Locate every Plasmodium vivax-infected red blood cell.
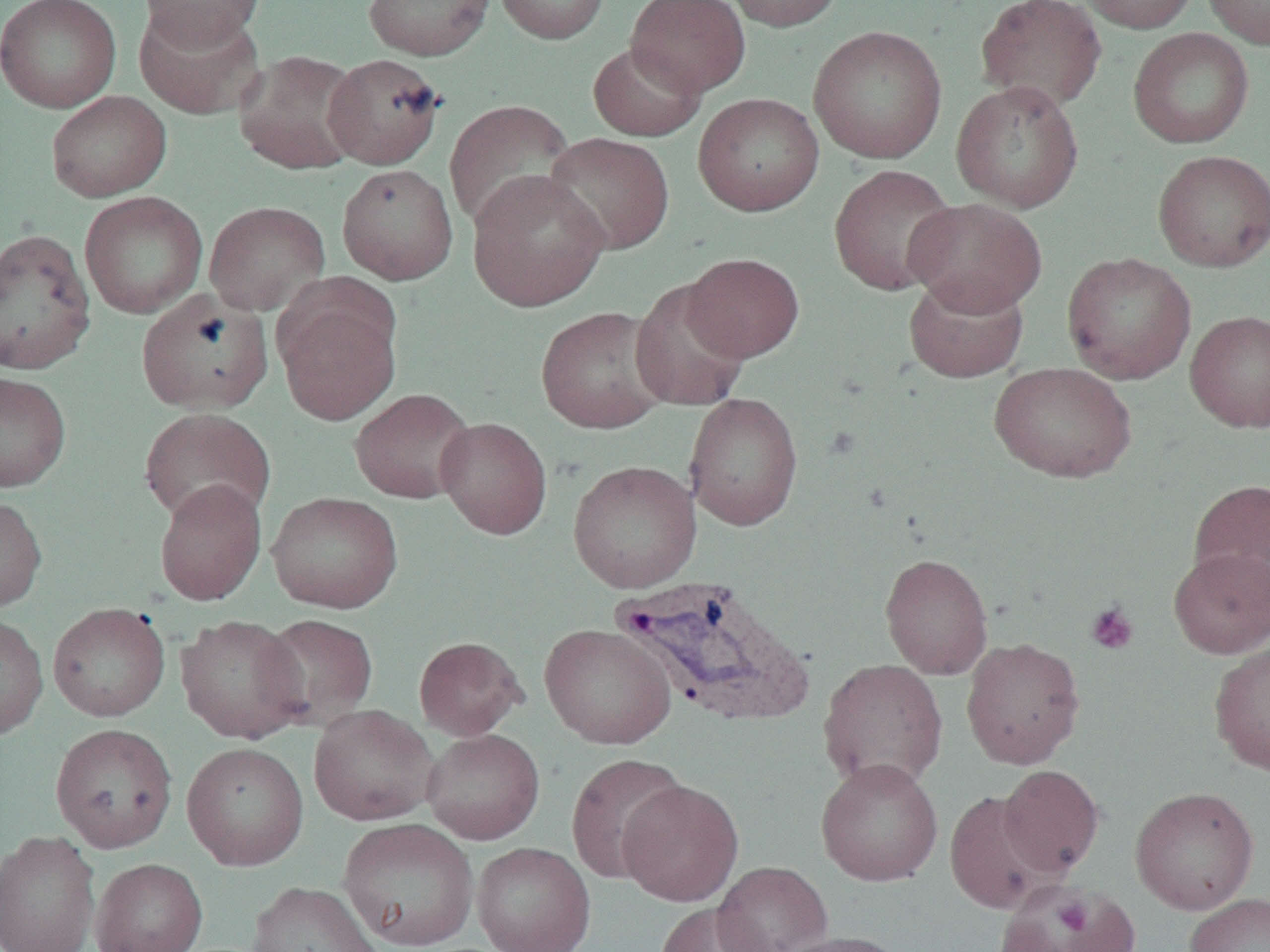
Approximate bounding boxes as [x1, y1, x2, y2] in pixels.
Plasmodium vivax-infected red blood cells: [610, 576, 815, 726].

slide-level diagnosis = Plasmodium vivax
magnification = 1000x
platelet locations = approximate bounding boxes as [x1, y1, x2, y2] in pixels: [1085, 602, 1139, 655], [1051, 895, 1097, 939]
modality = light microscopy
uninfected red blood cell locations = approximate bounding boxes as [x1, y1, x2, y2] in pixels: [0, 0, 122, 113], [138, 0, 267, 48], [362, 0, 496, 61], [493, 0, 611, 45], [626, 0, 751, 97], [723, 0, 846, 32], [974, 0, 1107, 113], [1077, 0, 1200, 34], [1202, 0, 1270, 49], [133, 3, 266, 119], [808, 26, 947, 164], [1128, 28, 1254, 149], [588, 41, 706, 142], [233, 49, 366, 175], [323, 52, 446, 169], [951, 79, 1084, 213], [46, 91, 172, 202], [693, 92, 824, 216], [444, 98, 576, 232], [542, 132, 675, 255], [1152, 149, 1270, 271], [336, 163, 458, 285], [828, 164, 959, 296], [466, 169, 610, 312], [79, 191, 207, 318], [902, 197, 1048, 317], [204, 201, 331, 316], [0, 228, 97, 375], [682, 252, 805, 362], [1061, 252, 1197, 385], [904, 273, 1029, 383], [630, 279, 752, 412], [136, 289, 273, 414], [275, 291, 401, 425], [535, 305, 673, 434], [1185, 309, 1270, 432], [989, 361, 1136, 483], [0, 370, 71, 492], [349, 388, 476, 504], [684, 392, 804, 531], [138, 407, 276, 527], [435, 416, 553, 540], [567, 460, 701, 593], [1187, 478, 1270, 607], [154, 479, 267, 606], [266, 491, 403, 614], [0, 494, 47, 613], [1168, 546, 1270, 658], [880, 552, 993, 679], [47, 602, 170, 721], [0, 613, 49, 741], [256, 613, 380, 730], [175, 614, 309, 744], [540, 623, 676, 748], [413, 635, 527, 739], [961, 637, 1085, 770], [1208, 639, 1270, 776], [818, 658, 948, 791], [308, 704, 440, 826], [50, 723, 178, 853], [421, 728, 545, 844], [181, 742, 309, 871], [566, 753, 689, 883], [815, 758, 944, 887], [998, 764, 1104, 877], [616, 779, 744, 906], [1130, 786, 1259, 915], [944, 790, 1058, 914], [338, 817, 478, 950], [0, 830, 101, 952], [471, 841, 596, 952], [90, 858, 207, 952], [713, 860, 833, 952], [248, 881, 382, 952], [998, 881, 1136, 952], [1184, 892, 1270, 952], [655, 903, 774, 952], [775, 930, 909, 952]
preparation = thin blood film
image size = 1270×952 pixels
field of view = single